Assess this cell for malaria.
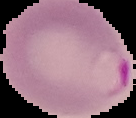

It is parasitized.

Summary:
  - Preparation: thin blood film
  - Image type: segmented cell region on a black background
  - Image size: 136×118 pixels